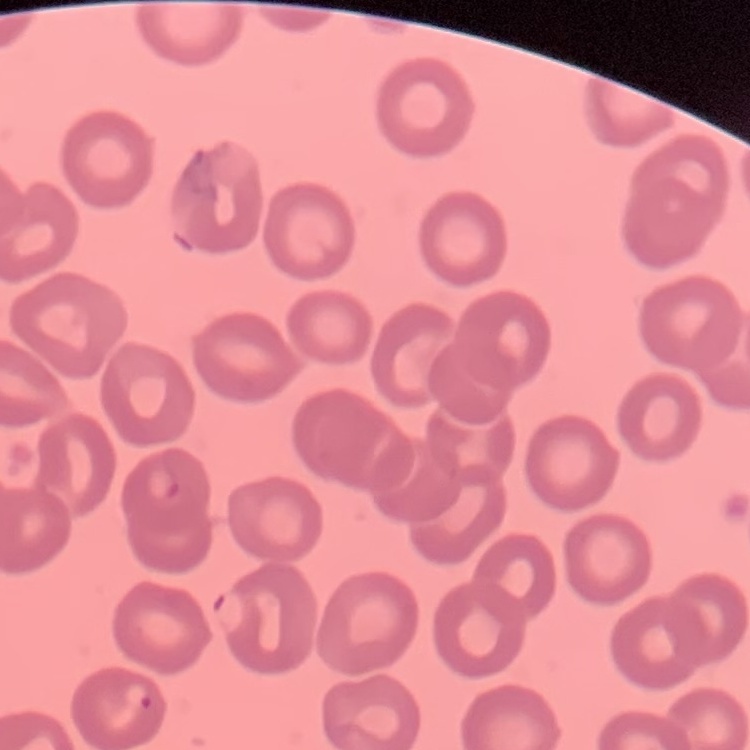
Summary:
  - Red blood cell morphology: no rouleaux formation
  - Preparation: thin peripheral smear
  - Stain: Field's or Giemsa
  - Image type: square crop of a larger photomicrograph